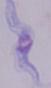
magnification = 1000x
identification = trypanosome
modality = micrograph